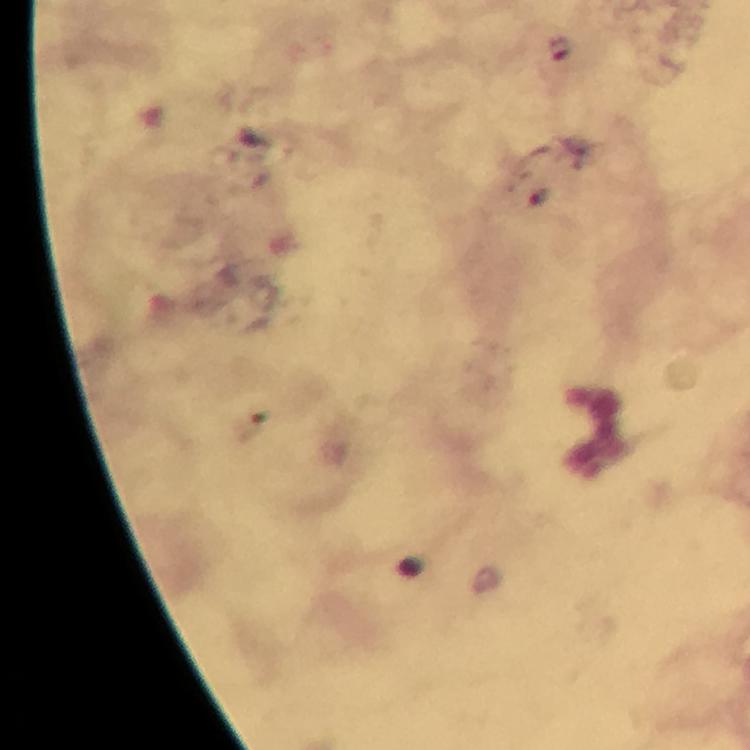

context = from a diagnostic examination for malaria
cropped from = one field of view
immersion oil = applied
image size = 750×750 pixels
magnification = 100x
stain = Giemsa
Plasmodium parasite locations = approximate object centers, in pixels from the top-left corner: (x=560, y=46), (x=540, y=196)
preparation = thick blood smear
capture = smartphone mounted on the microscope